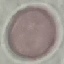
result = no malaria parasites detected
capture = smartphone camera at the microscope eyepiece
image type = automatically extracted cell patch, resized to 64 × 64 pixels
preparation = thin blood smear
stain = Giemsa